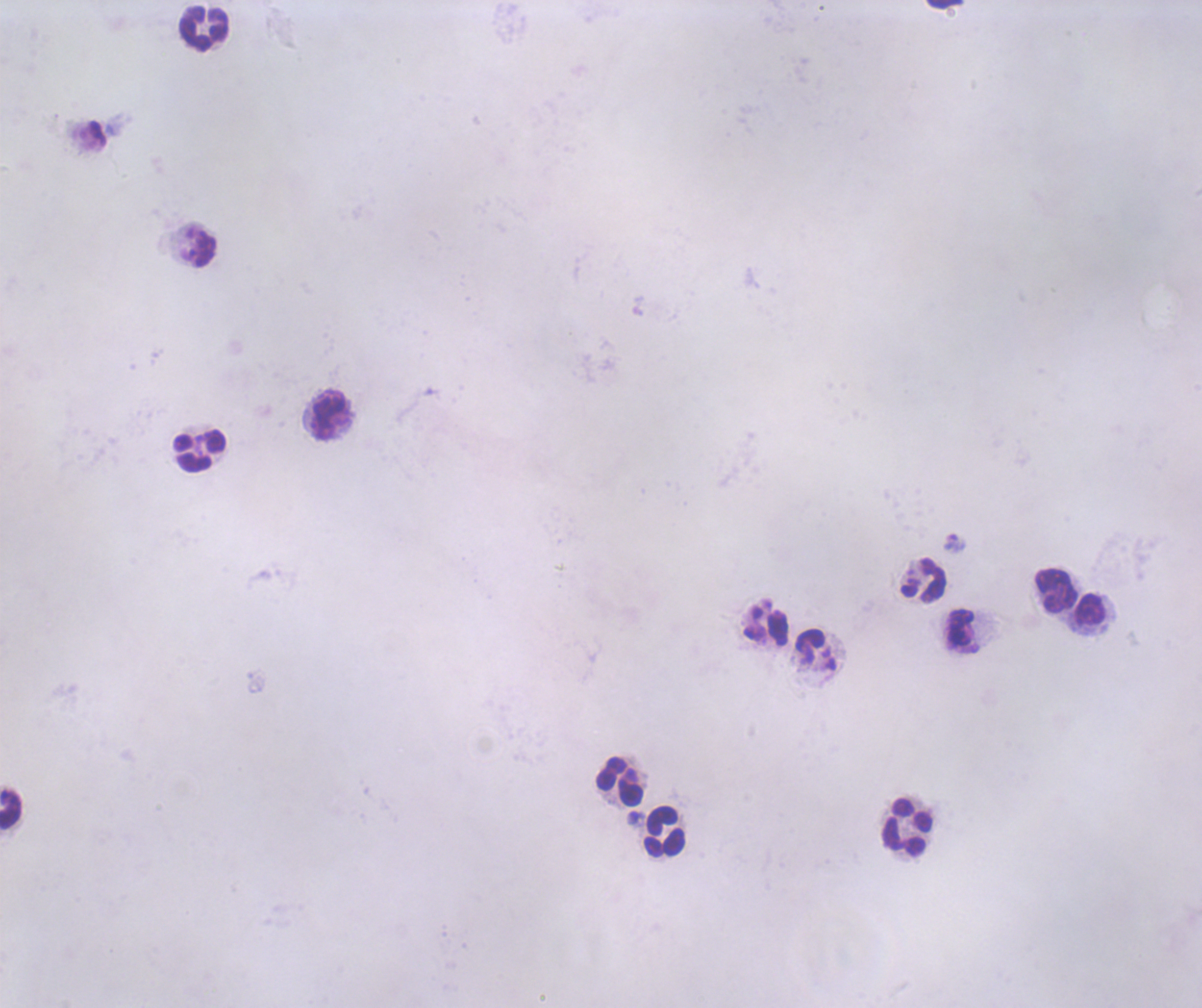

coordinate format = approximate object centers, in pixels from the top-left corner
leukocyte locations = (x=946, y=5), (x=204, y=28), (x=199, y=248), (x=330, y=415), (x=199, y=450), (x=924, y=579), (x=1056, y=590), (x=1091, y=609), (x=766, y=625), (x=960, y=627), (x=620, y=781), (x=11, y=808), (x=907, y=827), (x=666, y=831)
trophozoite locations = (x=954, y=543)
result = malaria parasites detected
coloration quality = bad
image size = 1202×1008 pixels
field of view = one from this slide
context = previously used in an actual diagnosis
stain = Romanowsky
background quality = unsatisfactory
magnification = 100x
preparation = thick smear of blood